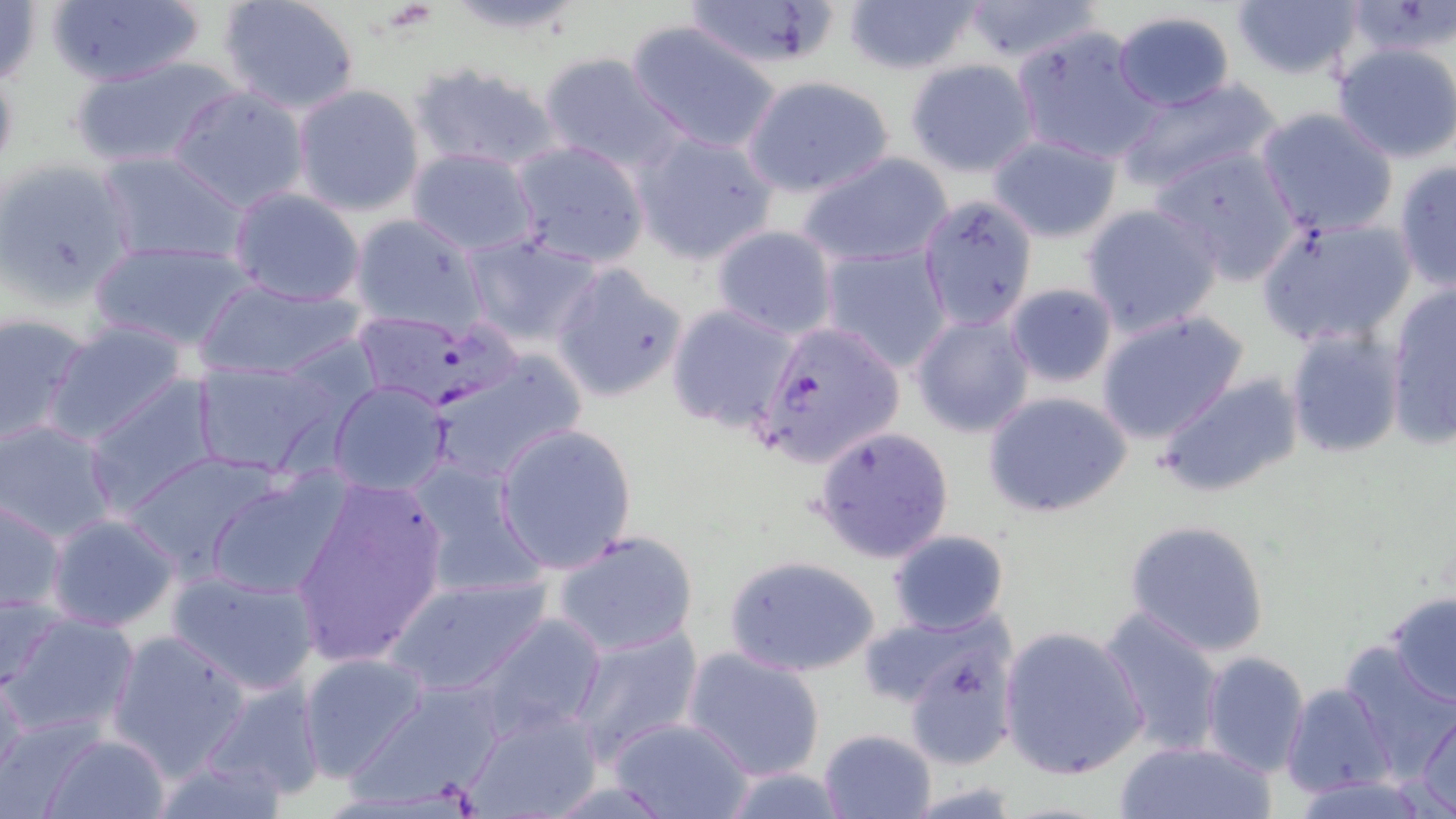

Approximate bounding boxes as (x1,y1)-(x2,y2) corner pairs in pixels. Uninfected red blood cell locations: (45,0)-(208,89), (217,0)-(362,115), (441,0)-(590,40), (679,0)-(843,74), (839,0)-(987,75), (959,0)-(1103,64), (0,1)-(46,88), (1230,1)-(1363,82), (1341,1)-(1456,64), (1110,11)-(1237,110), (624,19)-(782,153), (1012,23)-(1155,164), (1331,42)-(1456,165), (535,51)-(684,173), (65,54)-(246,171), (904,59)-(1040,177), (405,61)-(566,175), (743,76)-(895,197), (1114,76)-(1284,194), (290,83)-(425,216), (167,84)-(312,214), (1254,108)-(1399,237), (632,130)-(781,265), (987,134)-(1120,243), (509,139)-(651,268), (1153,144)-(1302,283), (406,146)-(541,257), (96,149)-(249,266), (797,152)-(954,268), (0,158)-(134,305), (1393,159)-(1455,291), (228,187)-(365,306), (917,191)-(1039,328), (1081,203)-(1225,337), (348,214)-(487,337), (1255,214)-(1415,350), (711,224)-(839,338), (463,233)-(604,346), (85,240)-(260,353), (819,244)-(954,373), (550,261)-(689,403), (191,276)-(369,382), (1004,281)-(1121,388), (1385,284)-(1455,445), (666,302)-(799,433), (1095,309)-(1249,445), (0,311)-(93,446), (911,311)-(1036,438), (41,320)-(193,447), (1284,326)-(1406,460), (428,352)-(587,485), (192,358)-(345,477), (1154,373)-(1301,500), (84,374)-(223,514), (326,380)-(455,495), (982,389)-(1135,520), (1,421)-(120,541), (495,423)-(637,575), (813,425)-(955,564), (120,451)-(287,579), (404,457)-(548,601), (204,472)-(352,600), (288,476)-(450,668), (1,495)-(67,614), (45,512)-(181,633), (1122,518)-(1273,658), (551,528)-(701,658), (887,529)-(1010,638), (723,554)-(881,678), (166,566)-(322,694), (384,573)-(552,698), (0,583)-(66,695), (1384,593)-(1456,708), (1096,606)-(1228,758), (3,611)-(140,738), (470,612)-(607,740), (565,624)-(704,763), (998,625)-(1149,781), (104,629)-(251,779), (899,639)-(1019,772), (1338,642)-(1456,775), (683,647)-(825,780), (1200,650)-(1310,777), (297,652)-(433,782), (0,669)-(28,790), (199,675)-(329,803), (343,680)-(510,806), (1280,681)-(1397,801), (463,703)-(604,819), (1413,707)-(1456,814), (605,715)-(754,819), (817,728)-(938,819), (36,732)-(173,819), (1111,740)-(1277,819), (145,749)-(294,819), (1289,776)-(1439,819). Platelet locations: (378,4)-(434,33). Plasmodium falciparum-infected red blood cell locations: (364,315)-(524,413), (751,319)-(904,471). Slide-level diagnosis: Plasmodium falciparum. 1000x magnification. Single field of view. May-Grünwald-Giemsa stain. Thin blood smear. Optical microscopy. Image is 1456×819 pixels.